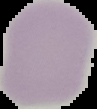

Summary:
  - Image size: 97×109 pixels
  - Image type: segmented cell region with the area outside set to black
  - Preparation: thin blood film
  - Result: no Plasmodium parasites detected